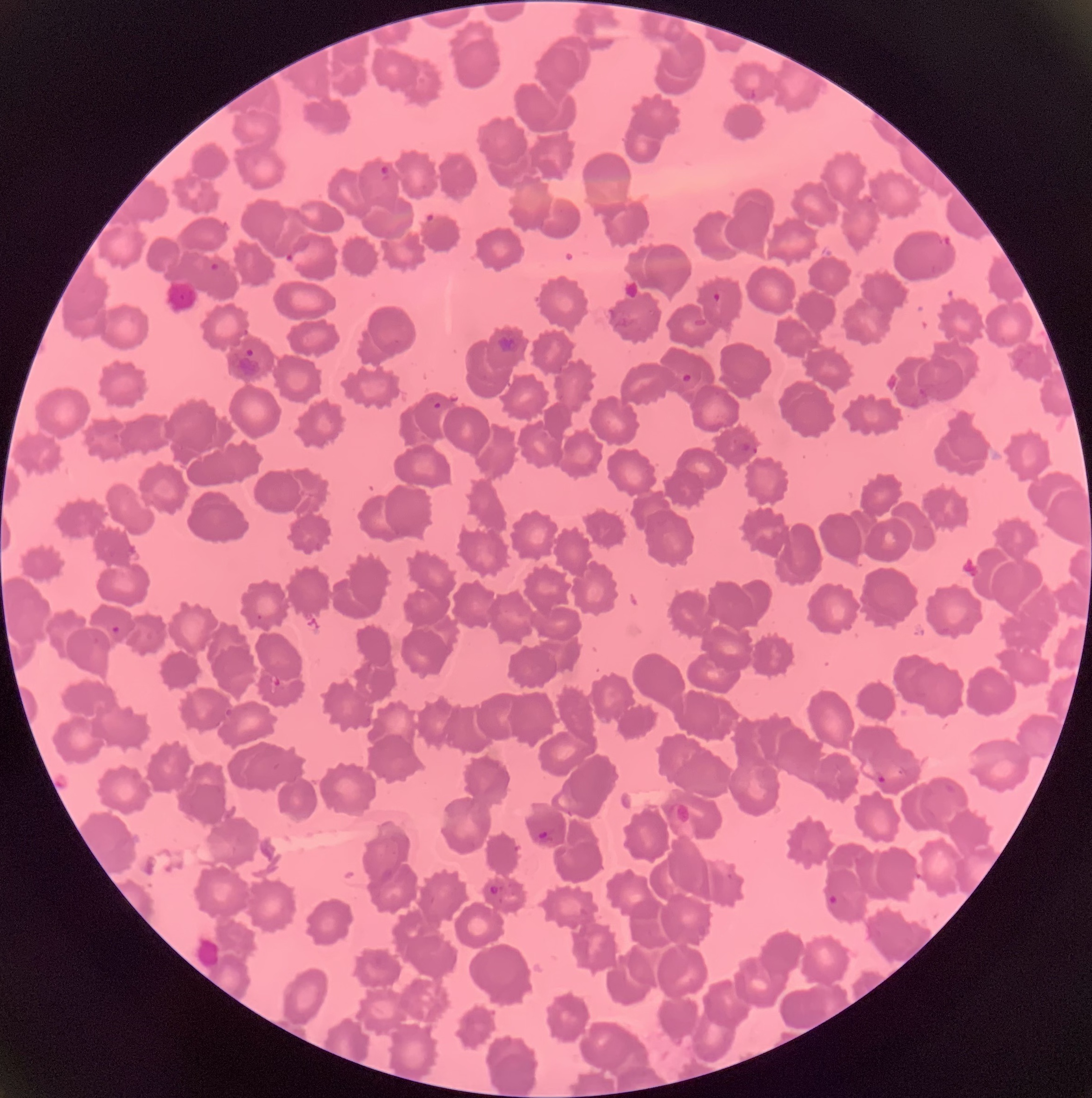
Summary:
  - Coordinate format: approximate bounding boxes as [x1, y1, x2, y2] in pixels
  - Plasmodium parasite locations: [379, 164, 392, 178], [424, 212, 440, 227], [285, 250, 308, 269], [209, 263, 220, 271], [712, 292, 721, 304], [244, 348, 255, 357], [681, 373, 692, 383], [431, 398, 443, 410], [742, 442, 758, 453], [109, 625, 122, 635], [270, 675, 282, 686], [876, 774, 887, 785], [535, 830, 549, 841], [488, 885, 501, 896], [828, 894, 839, 906]
  - Image size: 1092×1098 pixels
  - Modality: optical microscopy
  - Red blood cell morphology: rouleaux formation
  - Preparation: thin blood smear